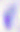 Captured at 400x magnification. Photomicrograph. Toxoplasma gondii is shown.